Classify this cell by malaria status.
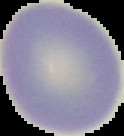

Uninfected.

From a thin blood film. The area outside the segmented cell region is set to black. Image is 124×136 pixels.